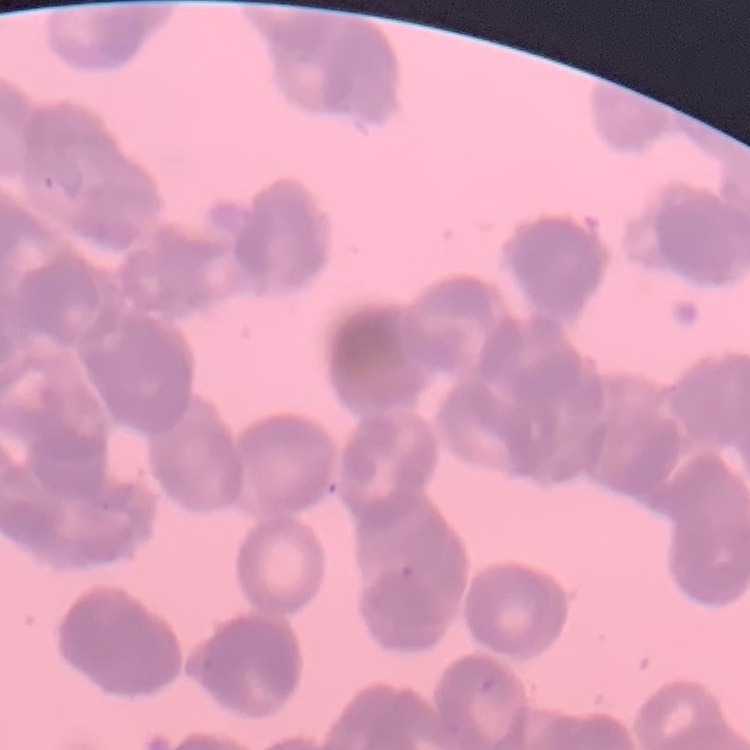

{
  "red_blood_cell_morphology": "rouleaux formation",
  "preparation": "thin blood smear",
  "image_type": "one tile cut from a larger photomicrograph",
  "stain": "Field's or Giemsa"
}